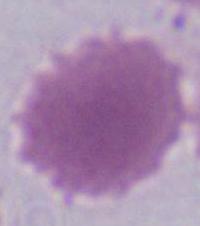
{
  "magnification": "1000x",
  "identification": "red blood cell",
  "modality": "micrograph"
}